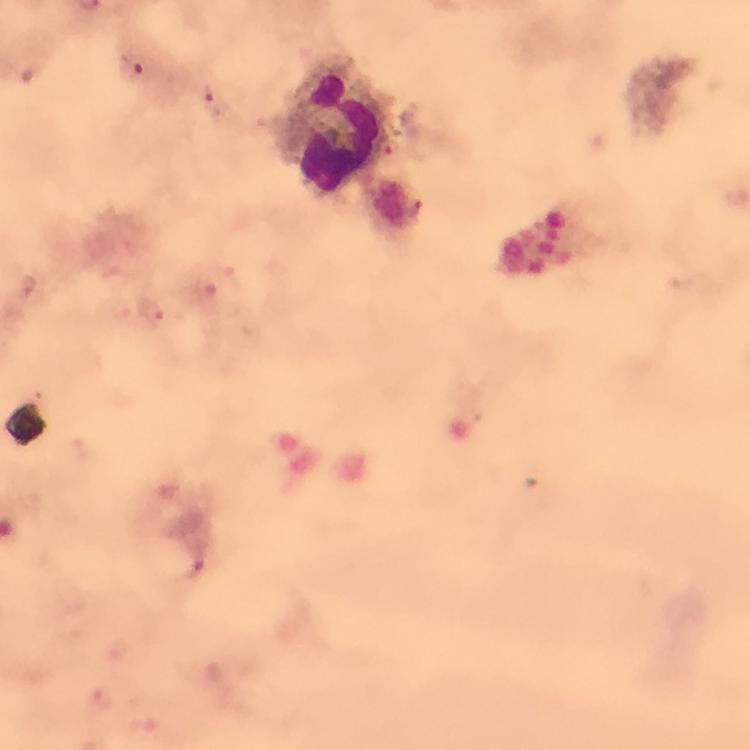

stain = Giemsa
magnification = 100x
immersion oil = used
leukocyte locations = approximate object centers, in pixels from the top-left corner: (x=334, y=127)
image size = 750×750 pixels
malaria parasite locations = approximate object centers, in pixels from the top-left corner: (x=137, y=65), (x=213, y=100), (x=154, y=314)
capture = smartphone camera through the microscope
preparation = thick blood smear
context = from a malaria diagnostic workup
cropped from = one field of view